Identify the cell.
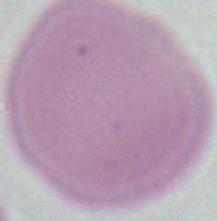
An erythrocyte.

Summary:
  - Magnification: 1000x
  - Modality: photomicrograph